Evaluate for malaria.
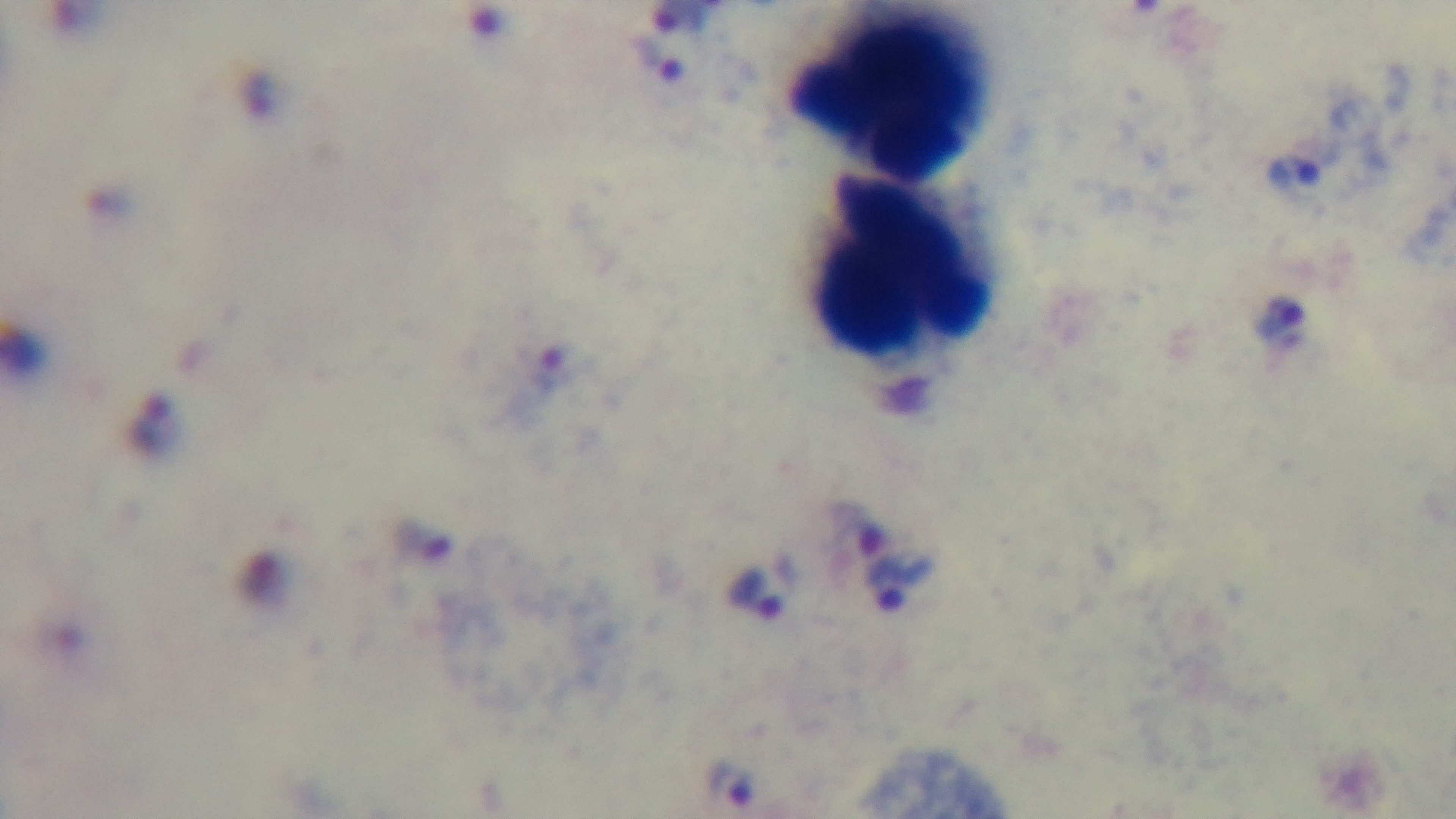
It is infected.

{
  "modality": "light microscopy",
  "objective": "100x oil immersion",
  "stain": "Giemsa",
  "capture": "mounted 4K digital camera",
  "preparation": "thick",
  "field_of_view": "single"
}